Assess this cell for malaria.
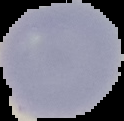

It is uninfected.

preparation = thin blood film
image type = segmented cell region on a black background
image size = 124×121 pixels